Report the malaria status of this cell.
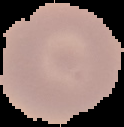

It is uninfected.

Image is 124×127 pixels. Cell region segmented out of the field of view; the surrounding area is masked to black. From a thin blood film.